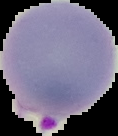

image_type: segmented cell region with the area outside set to black
malaria_status: parasitized
image_size: 118×136 pixels
preparation: thin blood smear